Locate every Plasmodium falciparum-infected red blood cell.
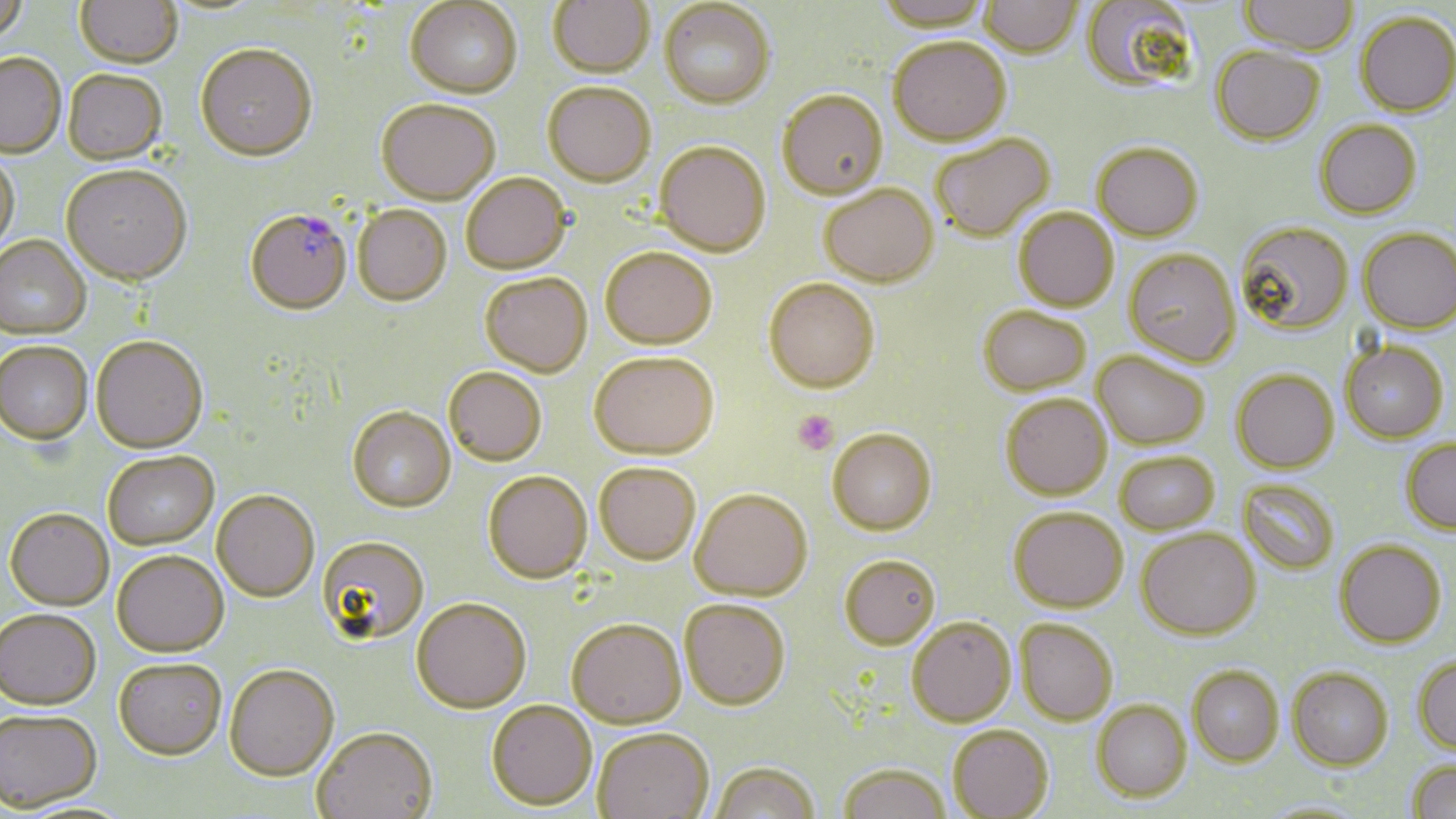

Approximate bounding boxes as named x1/y1/x2/y2 corners in pixels.
Plasmodium falciparum-infected red blood cells: (x1=246, y1=208, x2=352, y2=315).

{
  "slide_level_diagnosis": "Plasmodium falciparum",
  "field_of_view": "single",
  "image_size": "1456×819 pixels",
  "uninfected_red_blood_cell_locations": "approximate bounding boxes as named x1/y1/x2/y2 corners in pixels: (x1=0, y1=0, x2=28, y2=47), (x1=75, y1=0, x2=182, y2=69), (x1=549, y1=0, x2=654, y2=77), (x1=876, y1=0, x2=992, y2=33), (x1=979, y1=0, x2=1082, y2=59), (x1=1081, y1=0, x2=1200, y2=96), (x1=1239, y1=0, x2=1358, y2=58), (x1=406, y1=1, x2=523, y2=99), (x1=660, y1=1, x2=776, y2=108), (x1=1355, y1=13, x2=1456, y2=117), (x1=888, y1=36, x2=1011, y2=146), (x1=195, y1=43, x2=318, y2=162), (x1=1212, y1=47, x2=1325, y2=147), (x1=0, y1=53, x2=66, y2=158), (x1=63, y1=70, x2=167, y2=165), (x1=543, y1=82, x2=656, y2=186), (x1=777, y1=91, x2=888, y2=199), (x1=377, y1=98, x2=501, y2=205), (x1=1315, y1=120, x2=1421, y2=219), (x1=931, y1=134, x2=1055, y2=242), (x1=655, y1=141, x2=771, y2=257), (x1=1093, y1=143, x2=1204, y2=242), (x1=0, y1=152, x2=19, y2=255), (x1=61, y1=167, x2=192, y2=287), (x1=461, y1=173, x2=572, y2=274), (x1=819, y1=184, x2=938, y2=287), (x1=353, y1=204, x2=452, y2=306), (x1=1014, y1=207, x2=1119, y2=312), (x1=1235, y1=222, x2=1353, y2=335), (x1=1358, y1=227, x2=1456, y2=334), (x1=0, y1=236, x2=91, y2=340), (x1=601, y1=246, x2=717, y2=349), (x1=1124, y1=248, x2=1241, y2=367), (x1=480, y1=272, x2=592, y2=377), (x1=764, y1=277, x2=880, y2=393), (x1=978, y1=305, x2=1091, y2=395), (x1=91, y1=336, x2=208, y2=454), (x1=1341, y1=341, x2=1448, y2=442), (x1=0, y1=342, x2=93, y2=446), (x1=1092, y1=350, x2=1208, y2=450), (x1=589, y1=352, x2=718, y2=459), (x1=444, y1=367, x2=547, y2=466), (x1=1232, y1=369, x2=1339, y2=472), (x1=1001, y1=393, x2=1112, y2=500), (x1=347, y1=406, x2=455, y2=512), (x1=827, y1=427, x2=937, y2=535), (x1=1402, y1=439, x2=1456, y2=534), (x1=1114, y1=451, x2=1219, y2=534), (x1=102, y1=452, x2=219, y2=550), (x1=594, y1=462, x2=701, y2=564), (x1=483, y1=470, x2=593, y2=583), (x1=1238, y1=479, x2=1339, y2=574), (x1=690, y1=488, x2=812, y2=600), (x1=211, y1=490, x2=319, y2=601), (x1=1009, y1=508, x2=1129, y2=613), (x1=5, y1=509, x2=114, y2=610), (x1=1136, y1=528, x2=1260, y2=640), (x1=316, y1=535, x2=430, y2=645), (x1=1335, y1=539, x2=1446, y2=648), (x1=112, y1=550, x2=228, y2=657), (x1=840, y1=554, x2=940, y2=650), (x1=411, y1=597, x2=531, y2=712), (x1=680, y1=599, x2=791, y2=709), (x1=0, y1=609, x2=101, y2=709), (x1=567, y1=617, x2=686, y2=728), (x1=907, y1=617, x2=1016, y2=726), (x1=1015, y1=618, x2=1118, y2=725), (x1=1413, y1=655, x2=1456, y2=754), (x1=114, y1=657, x2=227, y2=761), (x1=224, y1=663, x2=339, y2=781), (x1=1188, y1=664, x2=1284, y2=766), (x1=1287, y1=666, x2=1393, y2=770), (x1=486, y1=700, x2=597, y2=810), (x1=1092, y1=700, x2=1191, y2=801), (x1=0, y1=707, x2=102, y2=813), (x1=948, y1=725, x2=1054, y2=819), (x1=312, y1=726, x2=439, y2=818), (x1=592, y1=727, x2=713, y2=819), (x1=1406, y1=759, x2=1456, y2=819), (x1=710, y1=761, x2=820, y2=819), (x1=838, y1=763, x2=951, y2=819), (x1=1257, y1=799, x2=1370, y2=817)",
  "platelet_locations": "approximate bounding boxes as named x1/y1/x2/y2 corners in pixels: (x1=793, y1=411, x2=838, y2=454)",
  "modality": "optical microscopy",
  "stain": "May-Grünwald-Giemsa",
  "preparation": "thin blood smear",
  "magnification": "1000x"
}